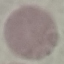

malaria status = uninfected
stain = Giemsa
preparation = thin blood smear
image type = cell patch, automatically extracted from a larger field of view and resized to 64 × 64 pixels
capture = smartphone camera at the microscope eyepiece